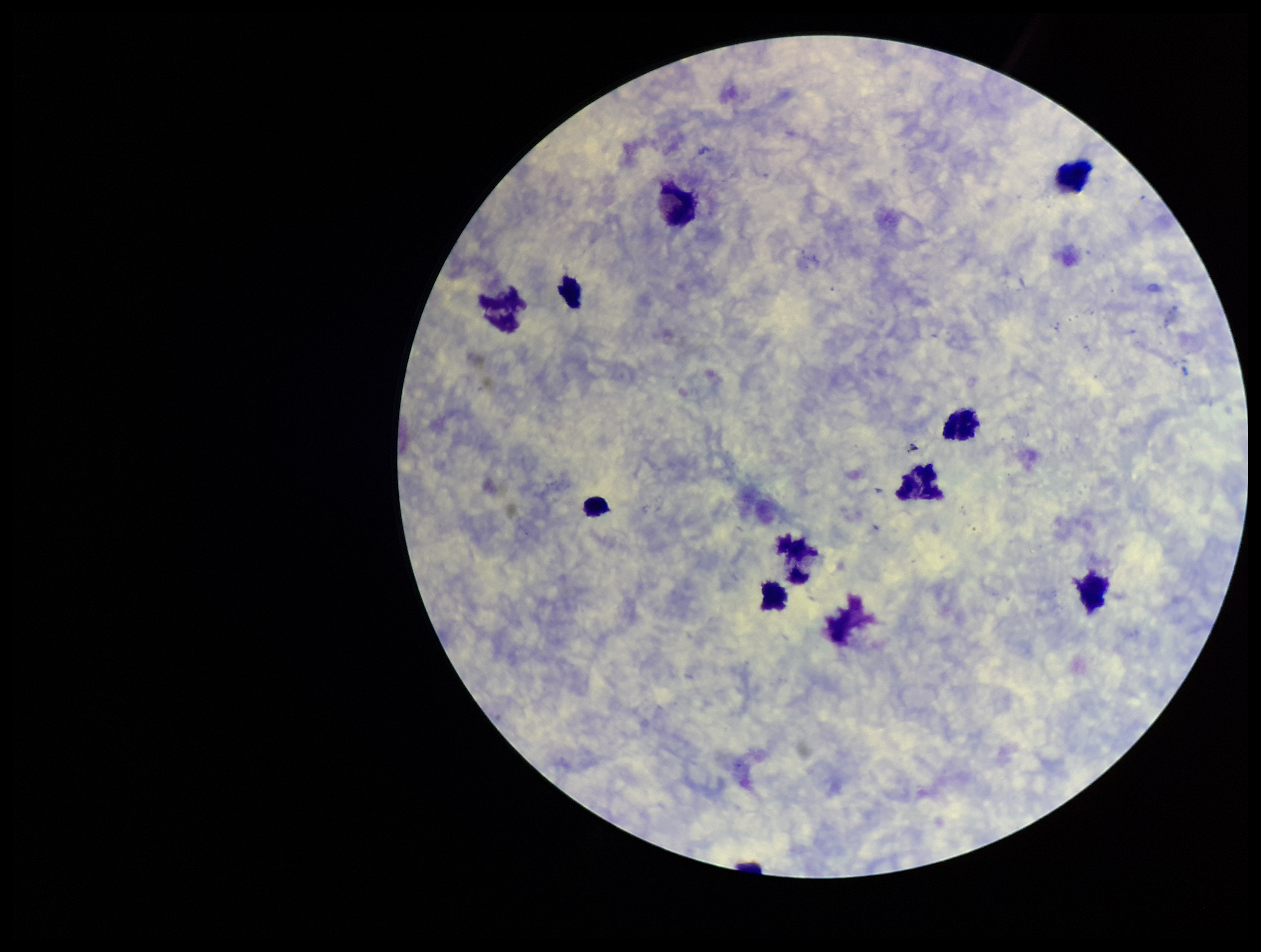

Single field of view. Patient malaria status: negative. Plasmodium parasites: none identified. Image is 1261×952 pixels. Smartphone photograph taken through the eyepiece of a microscope. Leukocyte count: 10. Parasite count: 0. Preparation: thick smear. Giemsa stain.